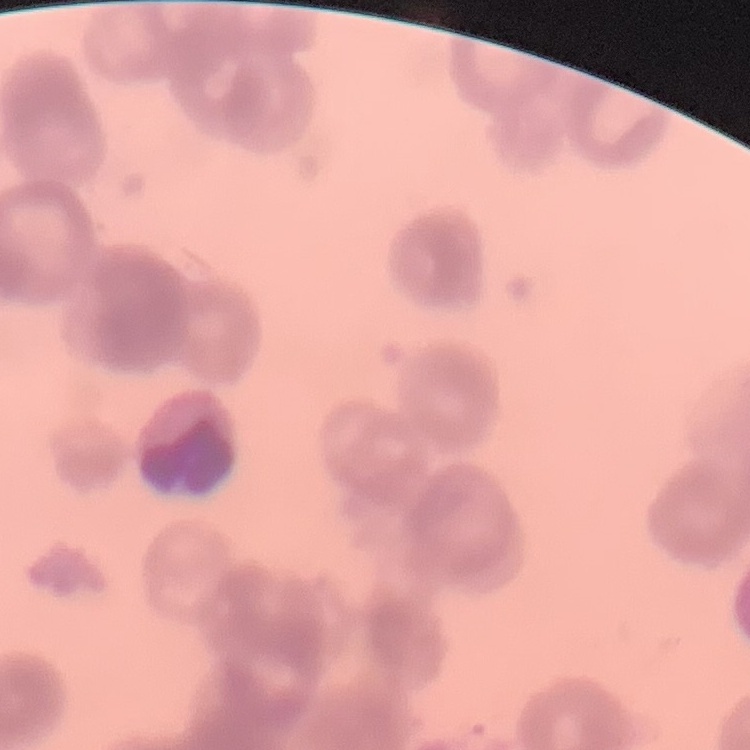
Summary:
  - Erythrocyte morphology: rouleaux formation
  - Preparation: thin blood film
  - Stain: Field's or Giemsa
  - Image type: one tile cut from a larger photomicrograph